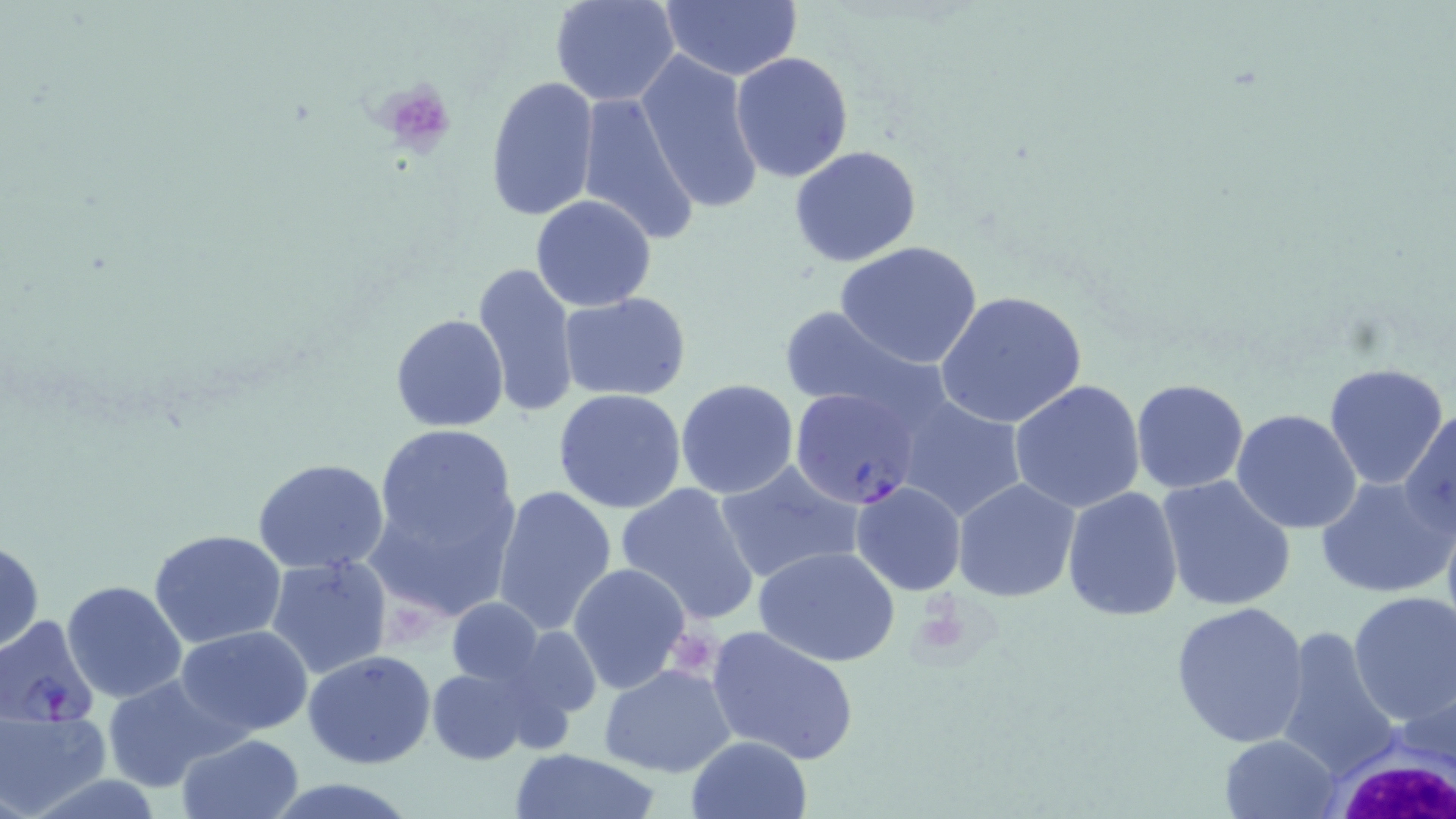
Plasmodium falciparum-infected red blood cell locations = approximate bounding boxes as (x1,y1)-(x2,y2) corner pairs in pixels: (791,388)-(923,509), (0,613)-(99,729)
slide-level diagnosis = Plasmodium falciparum
image size = 1456×819 pixels
modality = light microscopy
white blood cell locations = approximate bounding boxes as (x1,y1)-(x2,y2) corner pairs in pixels: (1328,745)-(1454,819)
field of view = one of a larger specimen
uninfected red blood cell locations = approximate bounding boxes as (x1,y1)-(x2,y2) corner pairs in pixels: (549,0)-(680,106), (658,0)-(805,82), (636,49)-(764,216), (731,51)-(854,182), (483,75)-(599,222), (575,90)-(699,245), (790,145)-(922,266), (531,194)-(657,312), (835,241)-(986,370), (473,260)-(580,419), (935,290)-(1087,432), (558,292)-(693,402), (776,304)-(933,417), (389,313)-(509,433), (1324,361)-(1449,490), (1130,377)-(1248,494), (675,379)-(799,498), (1008,379)-(1146,512), (553,388)-(688,514), (889,393)-(1028,523), (1402,408)-(1455,535), (1232,409)-(1362,533), (371,426)-(518,557), (251,458)-(392,573), (713,459)-(862,584), (1316,475)-(1452,598), (366,476)-(520,624), (1157,476)-(1297,611), (952,479)-(1081,603), (850,481)-(966,596), (615,482)-(761,624), (492,485)-(617,634), (1062,486)-(1183,621), (149,528)-(286,648), (0,540)-(45,652), (753,545)-(901,667), (265,555)-(394,681), (567,562)-(692,696), (61,579)-(187,705), (1347,591)-(1456,727), (446,599)-(542,685), (1170,600)-(1314,747), (175,625)-(315,738), (706,625)-(861,766), (1276,626)-(1400,782), (303,650)-(437,769), (599,664)-(737,778), (426,666)-(539,765), (100,673)-(234,793), (0,707)-(108,817), (177,734)-(304,819), (1219,734)-(1341,819), (685,736)-(812,819), (509,749)-(664,819), (262,778)-(422,818)
preparation = thin blood smear
platelet locations = approximate bounding boxes as (x1,y1)-(x2,y2) corner pairs in pixels: (375,79)-(460,158)
stain = May-Grünwald-Giemsa
magnification = 1000x